Look for Plasmodium parasites.
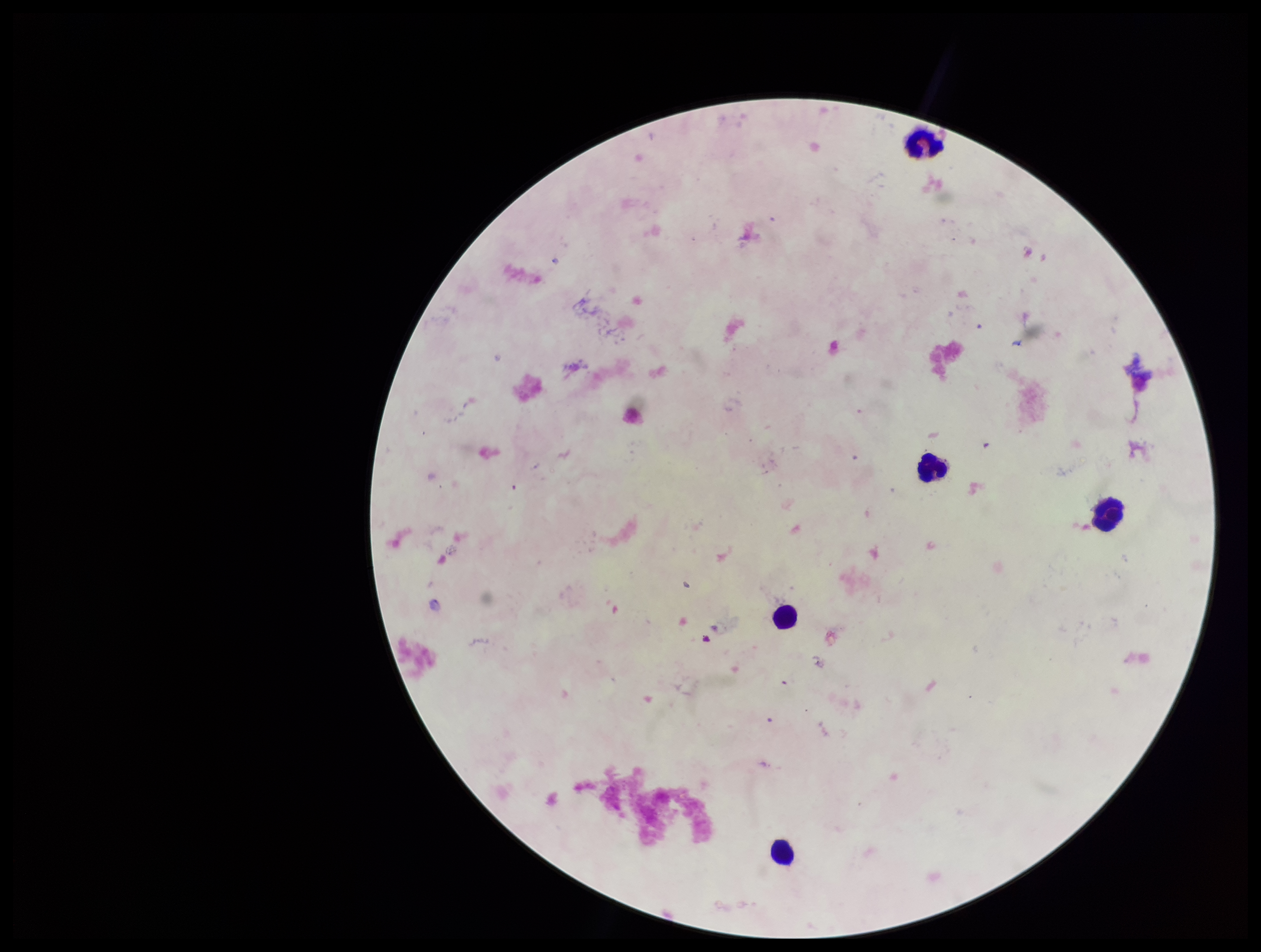
None identified.

capture: smartphone photograph through the microscope eyepiece
image_size: 1261×952 pixels
stain: Giemsa
field_of_view: single
preparation: thick smear
parasite_count: 0
leukocyte_count: 5
patient_malaria_status: negative